Comment on the morphology of the erythrocytes.
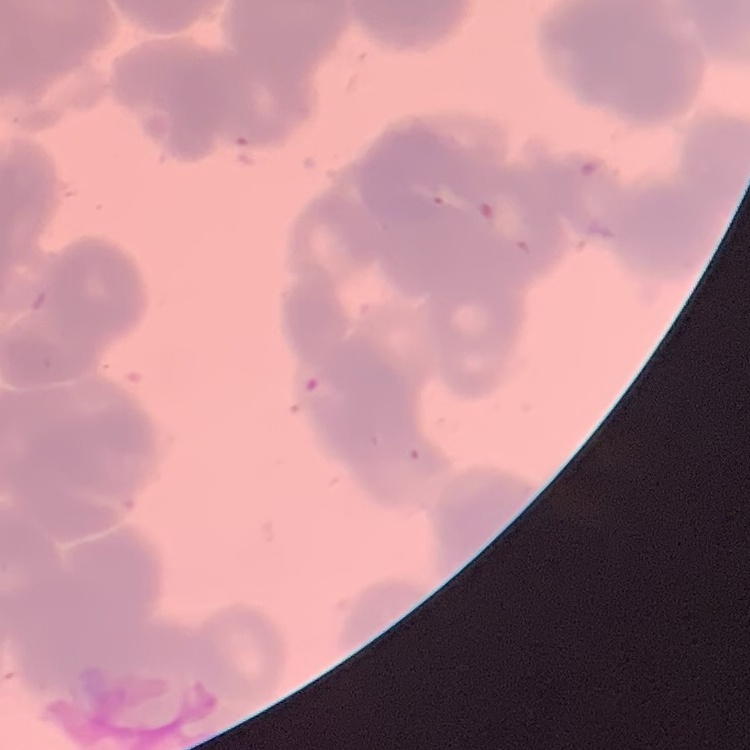

Rouleaux formation.

Summary:
  - Stain: Field's or Giemsa
  - Image type: one tile cut from a larger photomicrograph
  - Preparation: thin peripheral smear